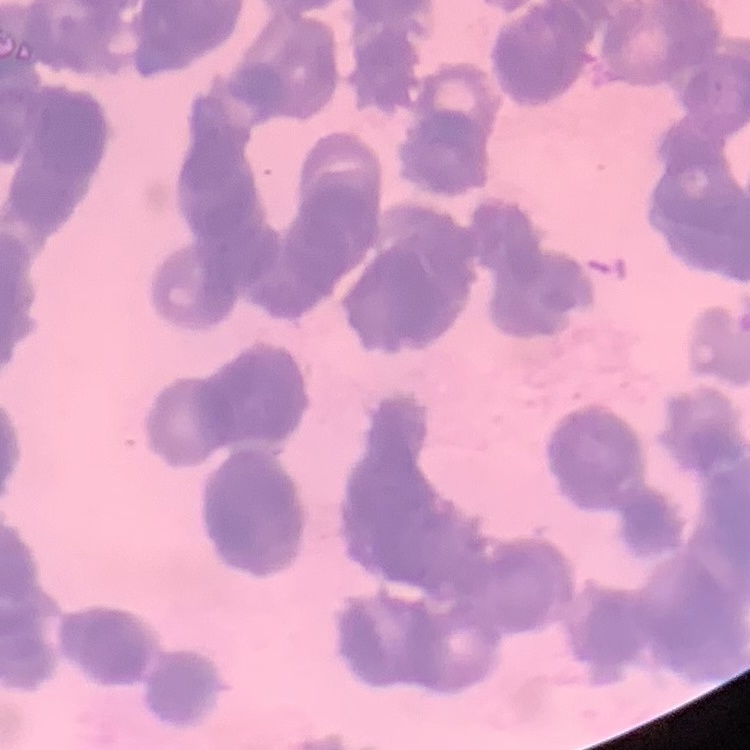

erythrocyte_morphology: rouleaux formation
preparation: thin blood smear
stain: Field's or Giemsa
image_type: square crop of a larger photomicrograph